Assess this cell for malaria.
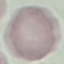

It is uninfected.

image_type: cell patch, automatically extracted from a larger field of view and resized to 64 × 64 pixels
preparation: thin blood smear
stain: Giemsa
capture: smartphone camera at the microscope eyepiece